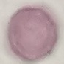
Malaria status: uninfected. Cell patch, automatically extracted from a larger field of view and resized to 64 × 64 pixels. Thin smear of blood. Acquired by smartphone through the microscope eyepiece. Giemsa stain.